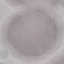 Result: no malaria parasites detected. Photographed with a smartphone camera at the microscope eyepiece. Thin blood film. Giemsa stain. Automatically extracted cell patch, resized to 64 × 64 pixels.